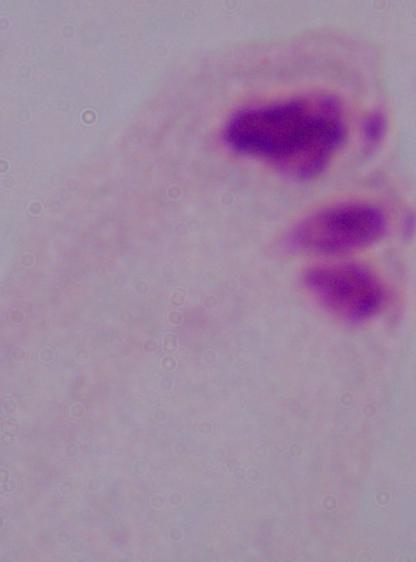

magnification = 1000x
identification = trichomonad
modality = micrograph